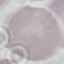
Malaria status: uninfected. Giemsa stain. Photographed with a smartphone camera at the microscope eyepiece. Thin smear of blood. Cell patch, automatically extracted from a larger field of view and resized to 64 × 64 pixels.